Assess this cell for malaria.
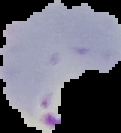
Parasitized.

image_size: 121×133 pixels
image_type: segmented cell region with the area outside set to black
preparation: thin blood film